Locate every white blood cell.
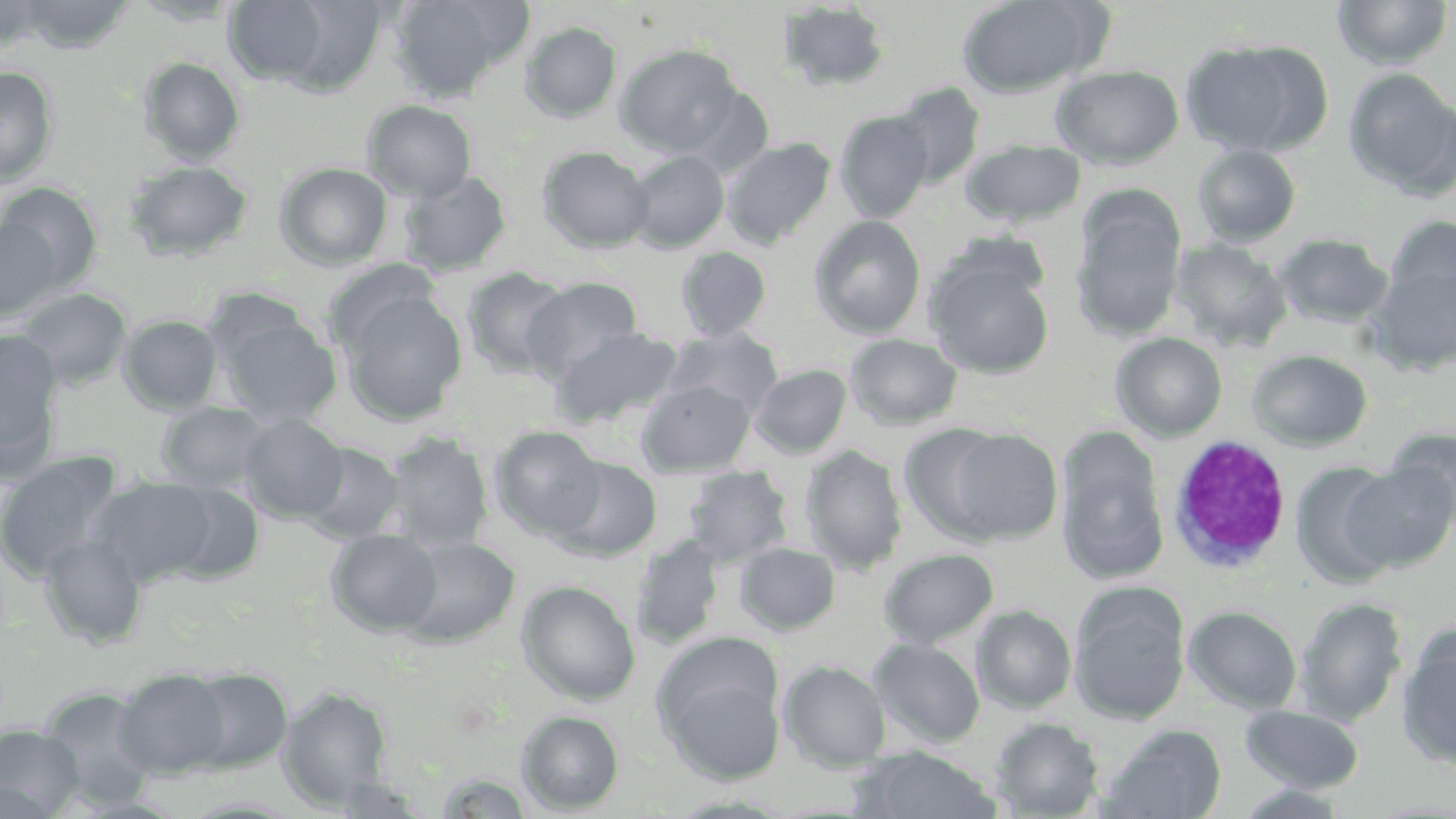
Approximate bounding boxes as [x1, y1, x2, y2] in pixels.
White blood cells: [1167, 435, 1292, 576].

slide-level diagnosis = no evidence of blood parasites
stain = May-Grünwald-Giemsa
uninfected red blood cell locations = approximate bounding boxes as [x1, y1, x2, y2] in pixels: [1, 0, 53, 51], [129, 0, 244, 26], [387, 0, 532, 102], [957, 0, 1110, 98], [1332, 0, 1453, 70], [14, 1, 137, 53], [221, 1, 353, 88], [777, 2, 890, 92], [520, 21, 622, 123], [1181, 39, 1329, 157], [616, 44, 742, 158], [138, 57, 246, 166], [0, 65, 59, 189], [1051, 65, 1184, 169], [1343, 68, 1456, 198], [893, 82, 985, 189], [682, 87, 774, 177], [362, 100, 477, 203], [834, 110, 935, 223], [722, 137, 837, 249], [961, 139, 1086, 228], [1192, 144, 1301, 248], [537, 146, 654, 253], [628, 151, 729, 253], [124, 160, 253, 263], [275, 162, 393, 271], [399, 170, 513, 277], [1, 182, 102, 293], [1073, 187, 1188, 343], [809, 215, 927, 339], [1384, 215, 1456, 312], [0, 219, 63, 323], [940, 230, 1050, 308], [1272, 232, 1393, 328], [1169, 238, 1293, 352], [675, 246, 771, 341], [926, 258, 1055, 378], [1366, 260, 1456, 375], [461, 267, 573, 379], [522, 277, 643, 381], [15, 286, 133, 389], [337, 290, 468, 425], [215, 308, 341, 427], [118, 315, 224, 415], [550, 326, 683, 427], [662, 327, 782, 417], [0, 329, 66, 480], [1111, 332, 1228, 441], [845, 333, 962, 431], [1247, 348, 1373, 452], [751, 364, 852, 458], [637, 380, 756, 477], [155, 401, 273, 493], [238, 413, 351, 522], [489, 425, 606, 541], [1384, 426, 1456, 530], [937, 427, 1064, 544], [1056, 430, 1170, 585], [380, 432, 494, 552], [301, 442, 405, 543], [800, 445, 908, 576], [0, 451, 123, 582], [551, 456, 662, 561], [1291, 460, 1407, 586], [1341, 460, 1456, 573], [683, 465, 794, 567], [90, 475, 228, 587], [153, 481, 267, 585], [326, 529, 442, 635], [632, 533, 726, 651], [39, 535, 148, 648], [396, 535, 520, 647], [734, 542, 841, 635], [879, 548, 999, 648], [516, 580, 640, 705], [1069, 585, 1191, 725], [1295, 596, 1408, 725], [972, 605, 1077, 713], [1184, 605, 1303, 714], [1396, 629, 1456, 770], [869, 638, 986, 748], [657, 653, 786, 787], [779, 660, 891, 771], [115, 668, 233, 778], [182, 669, 293, 774], [279, 686, 392, 808], [38, 687, 161, 807], [1241, 705, 1365, 793], [515, 710, 624, 814], [989, 716, 1105, 818], [1101, 724, 1228, 819], [0, 725, 84, 818], [854, 747, 1002, 819], [182, 796, 304, 817]
field of view = single
image size = 1456×819 pixels
modality = optical microscopy
magnification = 1000x
preparation = thin blood film